Assess this cell for malaria.
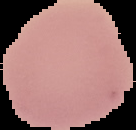

Uninfected.

Segmented cell region on a black background. Image is 136×130 pixels. From a thin blood smear.